Locate every Plasmodium parasite.
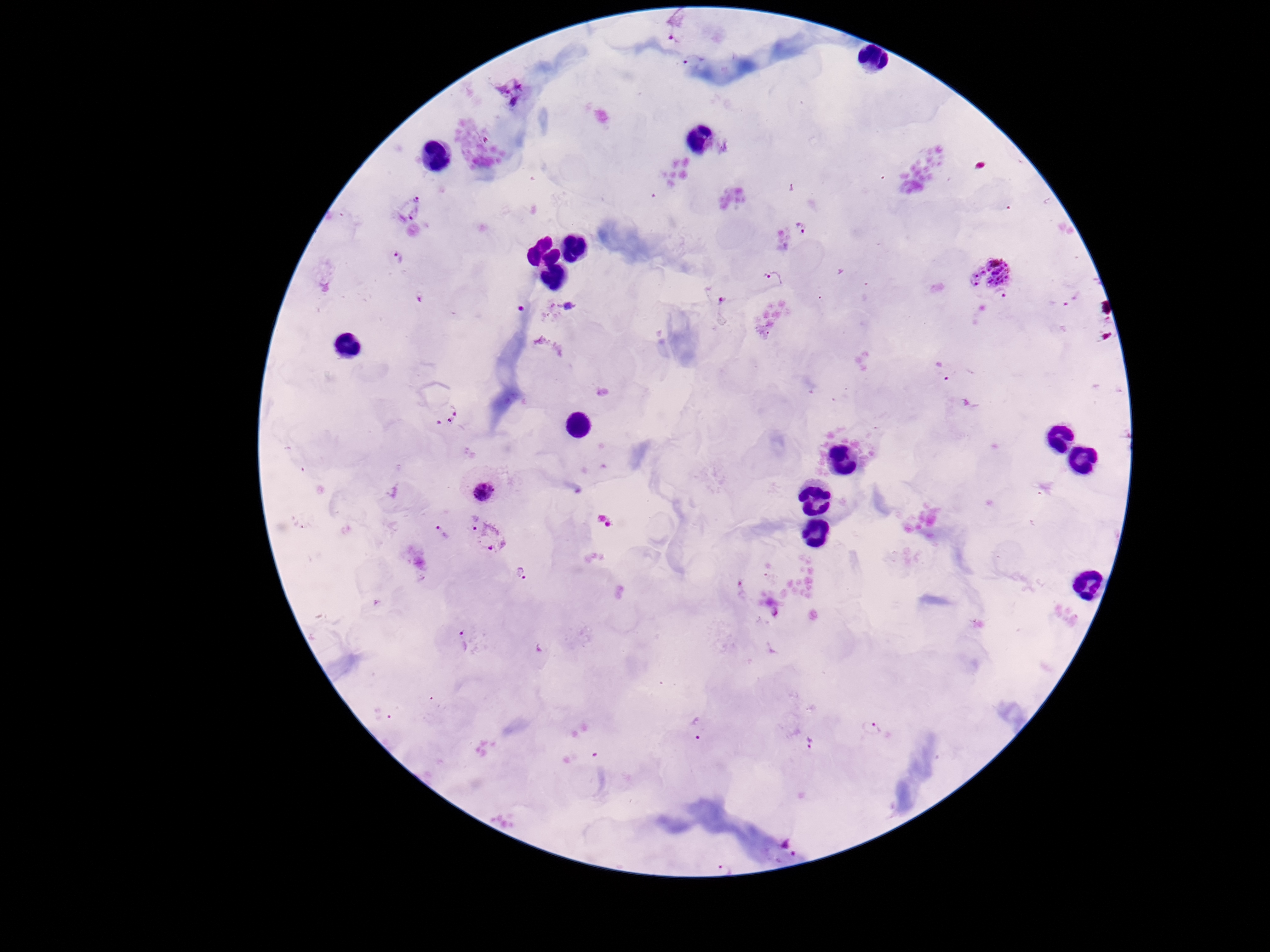
Approximate centers as [x, y] in pixels.
Plasmodium parasites: [678, 26], [694, 62], [510, 93], [409, 208], [805, 229], [398, 260], [989, 267], [773, 281], [716, 293], [1003, 296], [1071, 296], [568, 306], [943, 371], [448, 415], [483, 491], [469, 522], [443, 532], [494, 539], [525, 575], [466, 644], [696, 727], [873, 727], [810, 741], [788, 845].

stain = Giemsa
patient malaria status = infected
capture = smartphone camera through the microscope eyepiece
preparation = thick blood film
field of view = single
image size = 1270×952 pixels
magnification = 100x